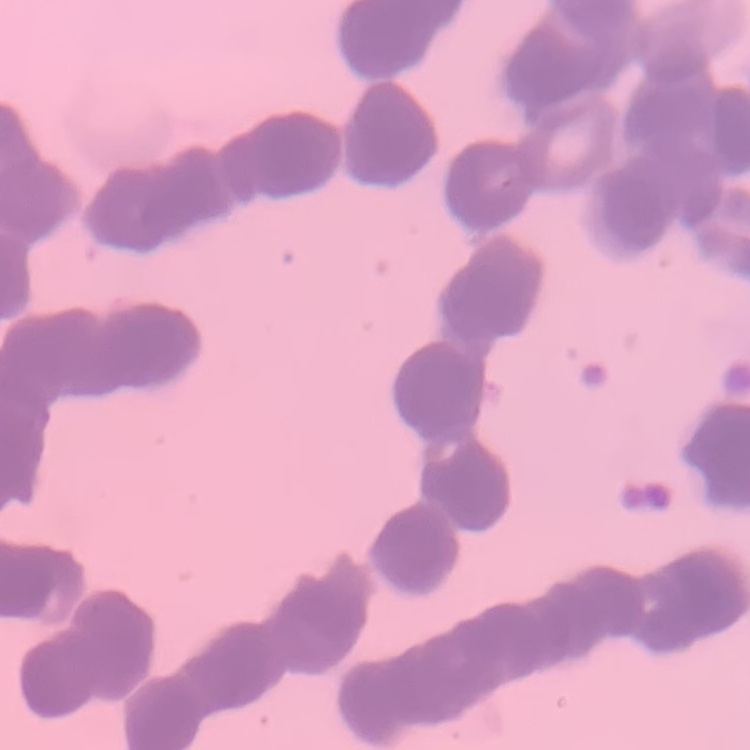

Summary:
  - Red blood cell morphology: rouleaux formation
  - Image type: one tile cut from a larger photomicrograph
  - Preparation: thin peripheral smear
  - Stain: Field's or Giemsa